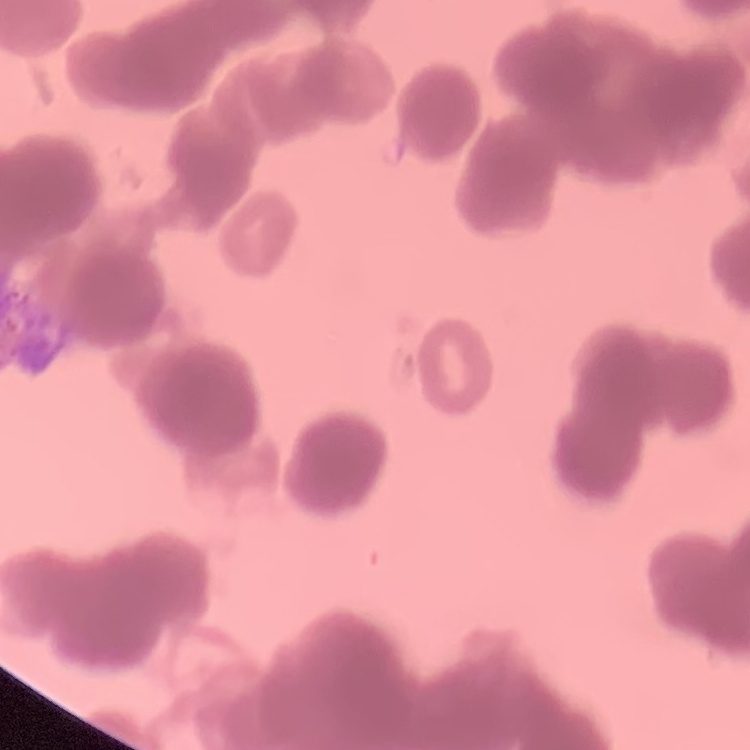
red_blood_cell_morphology: rouleaux formation
preparation: thin blood film
stain: Field's or Giemsa
image_type: one tile cut from a larger photomicrograph